State the blood parasite species.
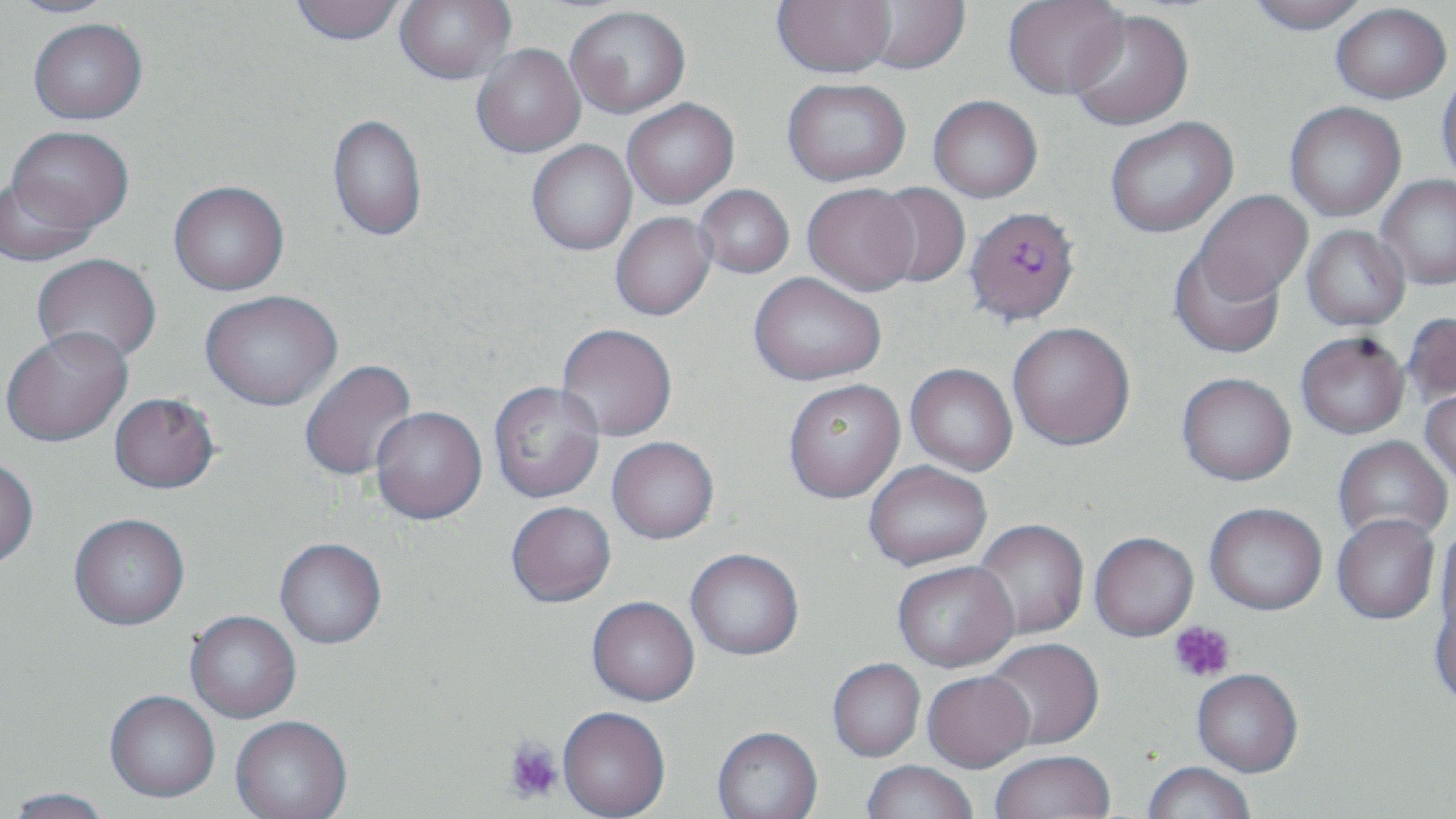

Plasmodium falciparum.

{
  "image_size": "1456×819 pixels",
  "preparation": "thin blood smear",
  "plasmodium_falciparum_infected_red_blood_cell_locations": "approximate bounding boxes as (x1,y1)-(x2,y2) corner pairs in pixels: (965,205)-(1080,325)",
  "uninfected_red_blood_cell_locations": "approximate bounding boxes as (x1,y1)-(x2,y2) corner pairs in pixels: (4,0)-(122,18), (290,0)-(406,46), (394,0)-(515,84), (773,0)-(896,77), (859,0)-(970,74), (1003,0)-(1128,99), (1246,0)-(1369,35), (1331,3)-(1451,103), (565,5)-(690,118), (1067,9)-(1194,131), (28,18)-(147,124), (471,44)-(585,157), (1436,70)-(1456,188), (783,78)-(910,186), (928,95)-(1042,202), (622,98)-(739,209), (1284,102)-(1406,221), (327,113)-(427,242), (1105,116)-(1238,238), (7,126)-(133,234), (527,140)-(637,256), (0,175)-(100,268), (1377,175)-(1456,289), (168,181)-(289,296), (802,183)-(920,296), (869,183)-(971,289), (695,185)-(794,279), (1194,190)-(1312,303), (611,212)-(716,321), (1301,225)-(1410,332), (1169,246)-(1286,359), (32,254)-(162,366), (748,272)-(886,385), (200,290)-(342,412), (1402,312)-(1456,410), (1008,322)-(1135,451), (556,324)-(677,442), (1,328)-(133,448), (1296,332)-(1410,439), (300,359)-(417,481), (905,363)-(1017,475), (1177,372)-(1296,485), (783,379)-(906,503), (489,381)-(605,504), (1420,388)-(1456,486), (109,395)-(219,497), (370,408)-(487,527), (1333,435)-(1452,545), (606,438)-(719,546), (0,458)-(39,571), (863,461)-(992,571), (507,503)-(616,610), (1205,503)-(1327,615), (1332,514)-(1440,624), (69,516)-(190,633), (972,519)-(1089,640), (1436,523)-(1455,639), (1089,533)-(1198,642), (275,540)-(387,651), (686,551)-(804,662), (892,563)-(1019,673), (587,599)-(700,708), (1429,599)-(1456,710), (185,612)-(301,724), (983,639)-(1105,751), (828,660)-(925,763), (1192,671)-(1302,778), (922,674)-(1035,775), (104,693)-(220,806), (557,709)-(671,819), (230,718)-(352,819), (712,728)-(823,819), (990,753)-(1114,818), (861,762)-(978,818), (1143,763)-(1254,819), (4,789)-(115,819)",
  "field_of_view": "single",
  "stain": "May-Grünwald-Giemsa",
  "modality": "optical microscopy",
  "platelet_locations": "approximate bounding boxes as (x1,y1)-(x2,y2) corner pairs in pixels: (1169,621)-(1236,683), (504,737)-(564,804)",
  "magnification": "1000x"
}